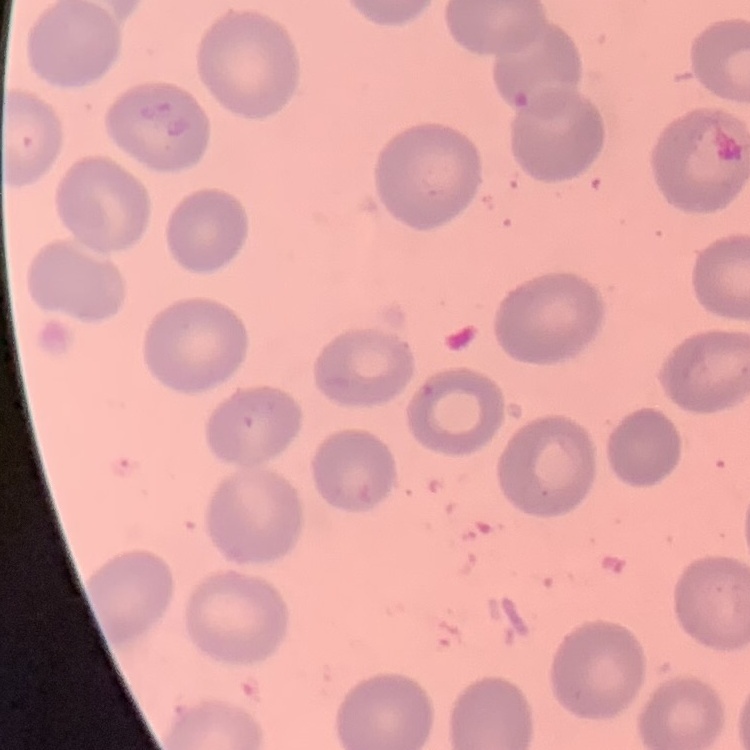
Summary:
  - Erythrocyte morphology: no rouleaux formation
  - Preparation: thin blood film
  - Image type: one tile cut from a larger photomicrograph
  - Stain: Field's or Giemsa